Classify this cell by malaria status.
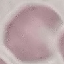
Uninfected.

Thin smear of blood. Cell patch, automatically extracted from a larger field of view and resized to 64 × 64 pixels. Giemsa-stained preparation. Acquired by smartphone through the microscope eyepiece.